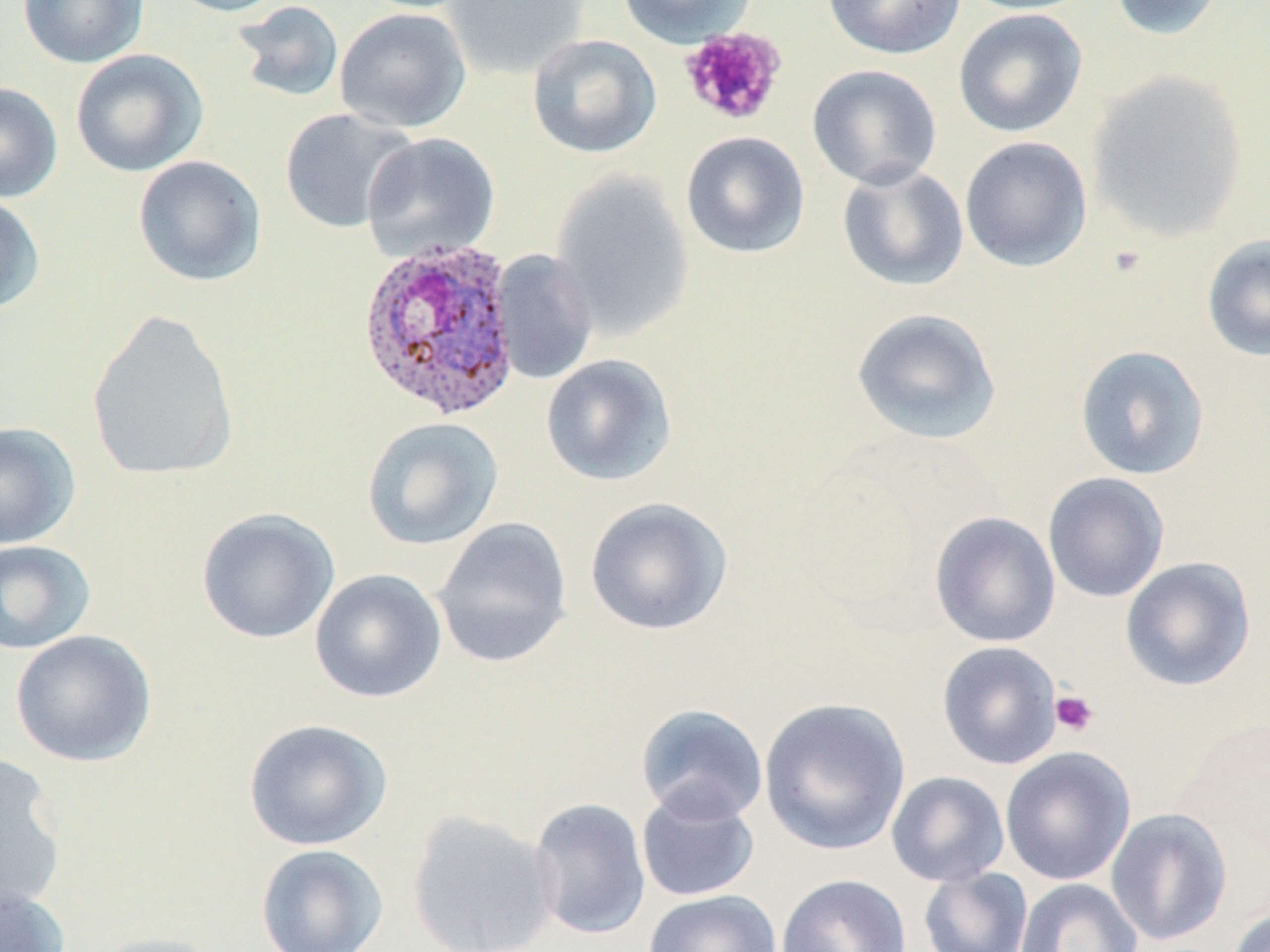

slide-level diagnosis = Plasmodium ovale
platelet locations (subset) = approximate bounding boxes as (x1, y1, x2, y2) in pixels: (1049, 690, 1098, 736)
uninfected red blood cell locations (subset) = approximate bounding boxes as (x1, y1, x2, y2) in pixels: (17, 0, 149, 69), (160, 0, 292, 18), (352, 0, 483, 13), (442, 0, 589, 80), (618, 0, 755, 48), (822, 0, 966, 60), (954, 0, 1095, 16), (1106, 0, 1227, 42), (231, 1, 345, 104), (334, 7, 472, 133), (953, 9, 1087, 138), (526, 33, 662, 159), (70, 49, 207, 176), (807, 65, 942, 190), (1086, 70, 1250, 242), (0, 82, 63, 202), (279, 108, 417, 234), (680, 131, 810, 259), (363, 132, 500, 261), (959, 136, 1093, 272), (132, 155, 267, 287), (836, 163, 970, 292), (551, 171, 695, 341), (0, 194, 46, 314), (1202, 233, 1270, 363), (491, 249, 599, 385), (851, 307, 1002, 445), (86, 309, 240, 482), (1075, 344, 1210, 481), (540, 354, 677, 486), (361, 416, 504, 551), (0, 421, 80, 549), (1042, 472, 1170, 603), (584, 496, 733, 636), (196, 507, 339, 644), (929, 512, 1061, 648), (432, 517, 573, 668), (0, 539, 96, 654), (1120, 556, 1257, 692), (309, 568, 448, 704), (10, 629, 157, 768), (936, 641, 1063, 770), (758, 696, 911, 856), (635, 703, 768, 824), (242, 718, 393, 851), (1000, 746, 1136, 885), (0, 752, 68, 915), (886, 771, 1010, 887), (636, 788, 761, 902), (528, 797, 651, 940), (1105, 807, 1233, 946), (405, 809, 560, 952), (255, 844, 388, 952), (918, 867, 1034, 952), (775, 873, 911, 952), (1014, 878, 1143, 952), (0, 883, 69, 952), (643, 889, 782, 952), (1226, 906, 1269, 952), (89, 931, 228, 952)
modality = light microscopy
image size = 1270×952 pixels
preparation = thin blood smear
magnification = 1000x
Plasmodium ovale-infected red blood cell locations = approximate bounding boxes as (x1, y1, x2, y2) in pixels: (357, 238, 521, 423)
stain = May-Grünwald-Giemsa
field of view = single